Give the position of every Plasmodium parasite visible.
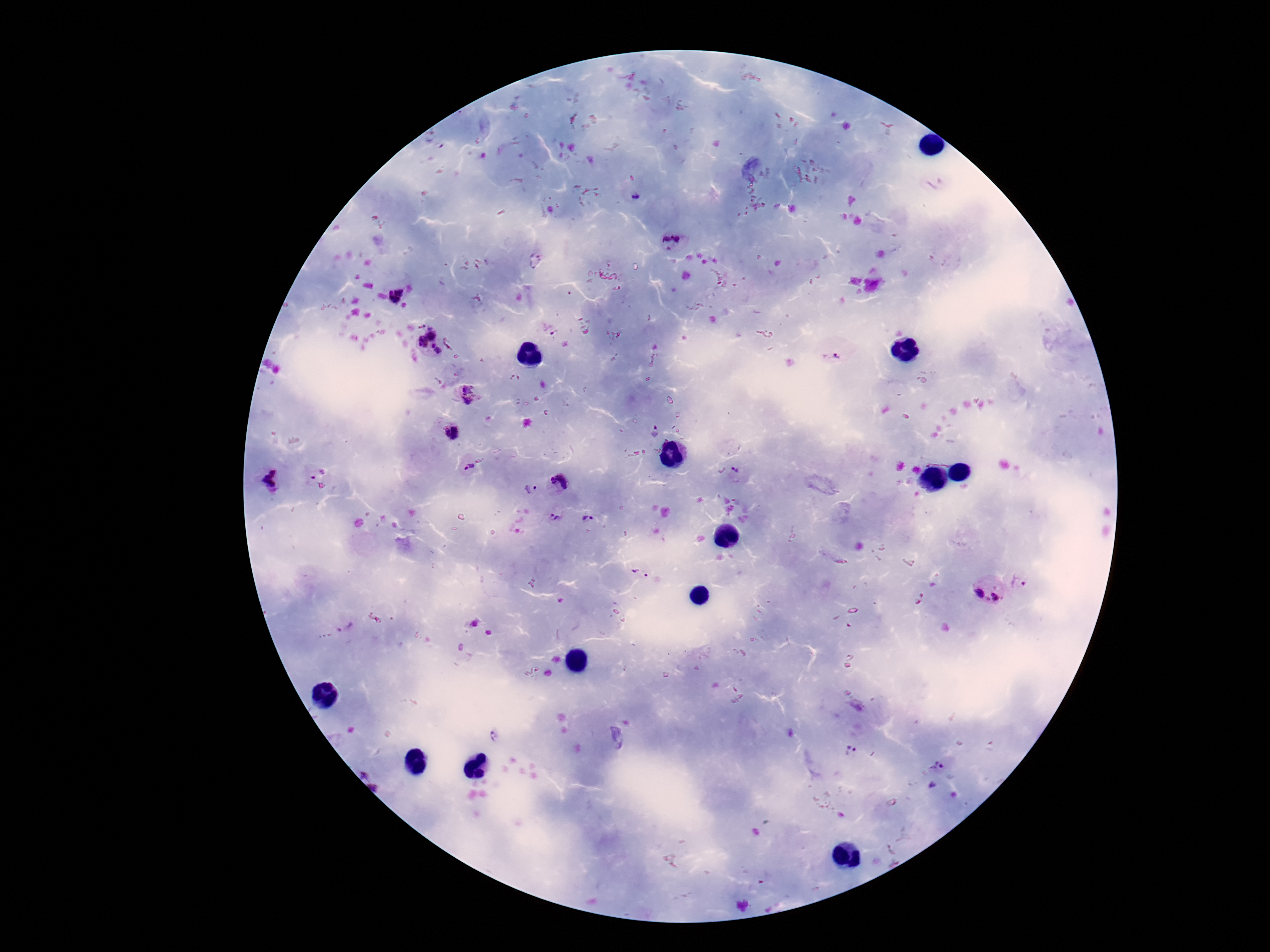

Approximate centers as {x, y} in pixels.
Plasmodium parasites: {636, 198}, {672, 241}, {395, 294}, {421, 326}, {554, 330}, {432, 333}, {422, 342}, {436, 349}, {831, 358}, {467, 394}, {654, 432}, {451, 433}, {469, 467}, {736, 470}, {315, 473}, {271, 479}, {560, 480}, {530, 489}, {554, 517}, {588, 518}, {640, 574}, {1021, 582}, {978, 594}, {996, 598}, {345, 628}, {532, 671}, {493, 735}, {852, 745}, {938, 764}.

Summary:
  - Image size: 1270×952 pixels
  - Field of view: single
  - Magnification: 100x
  - Preparation: thick blood smear
  - Stain: Giemsa
  - Capture: smartphone camera through the microscope eyepiece
  - Patient malaria status: infected